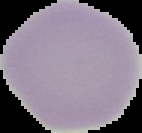
preparation = thin blood smear
image type = cell region segmented out of the field of view; surrounding area masked to black
malaria status = uninfected
image size = 142×133 pixels